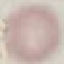

Summary:
  - Result: negative for malaria parasites
  - Stain: Giemsa
  - Image type: automatically extracted cell patch, resized to 64 × 64 pixels
  - Capture: smartphone camera at the microscope eyepiece
  - Preparation: thin blood smear